Classify this cell by malaria status.
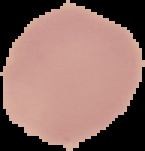
It is uninfected.

Summary:
  - Image type: cell region segmented out of the field of view; surrounding area masked to black
  - Image size: 145×151 pixels
  - Preparation: thin blood smear